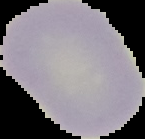

Summary:
  - Image type: segmented cell region on a black background
  - Image size: 145×139 pixels
  - Preparation: thin blood smear
  - Malaria status: uninfected